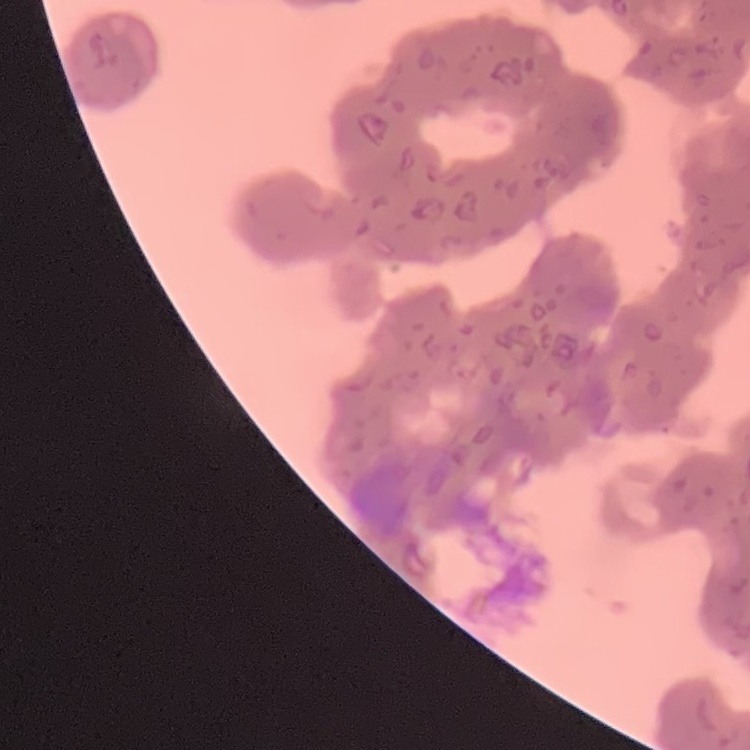

erythrocyte morphology = rouleaux formation
stain = Field's or Giemsa
image type = one tile cut from a larger photomicrograph
preparation = thin peripheral smear